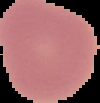

{
  "image_size": "100×103 pixels",
  "image_type": "segmented cell region with the area outside set to black",
  "preparation": "thin blood film",
  "malaria_status": "uninfected"
}